Locate every Plasmodium parasite.
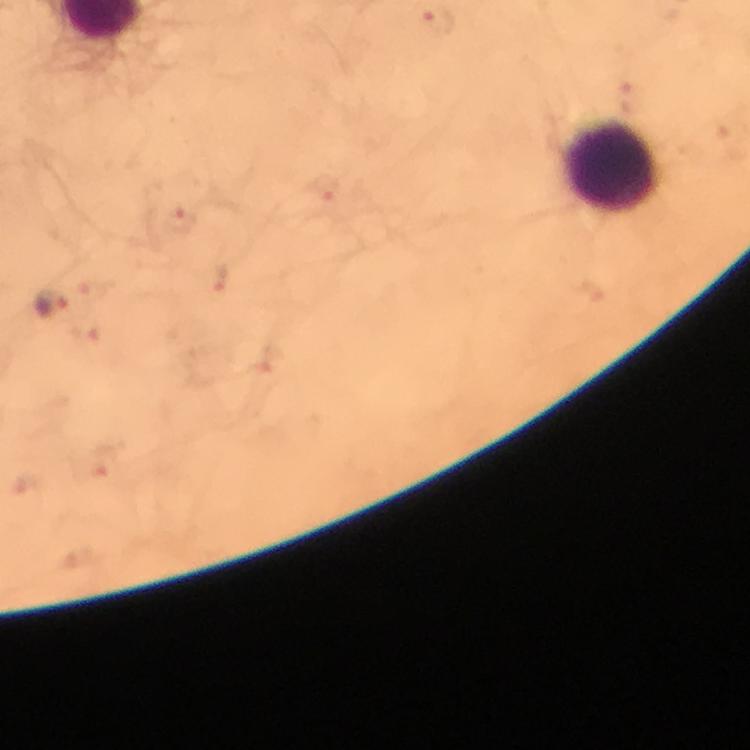

Approximate centers as {x, y} in pixels.
Plasmodium parasites: {334, 194}, {181, 221}, {219, 280}, {50, 303}, {101, 462}.

Leukocyte locations: {614, 166}. Immersion oil was used. Giemsa-stained preparation. A crop from one field of view. Image is 750×750 pixels. Photographed with a smartphone mounted on the microscope. From a malaria diagnostic workup. 100x magnification. Thick blood smear.